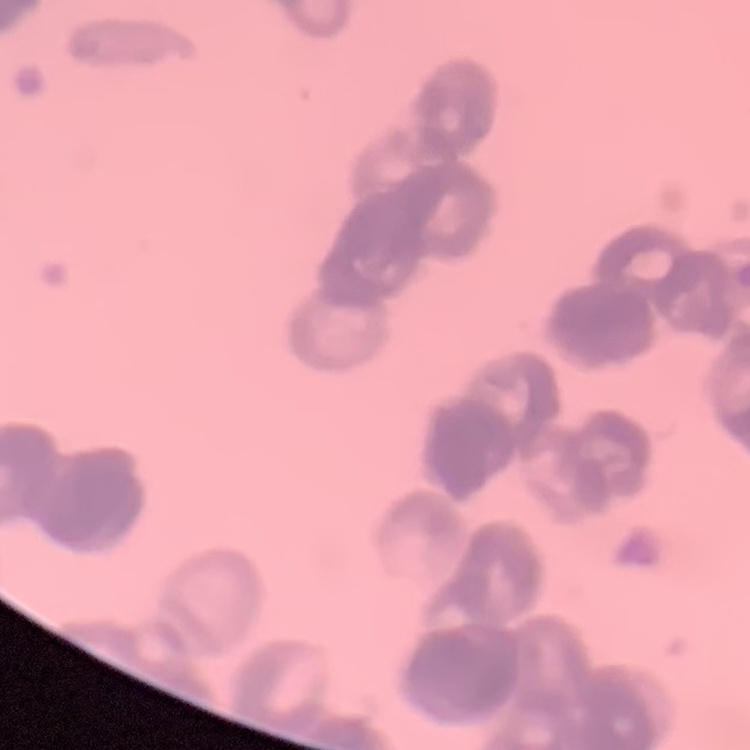

Summary:
  - Erythrocyte morphology: rouleaux formation
  - Image type: square crop of a larger photomicrograph
  - Stain: Field's or Giemsa
  - Preparation: thin peripheral smear